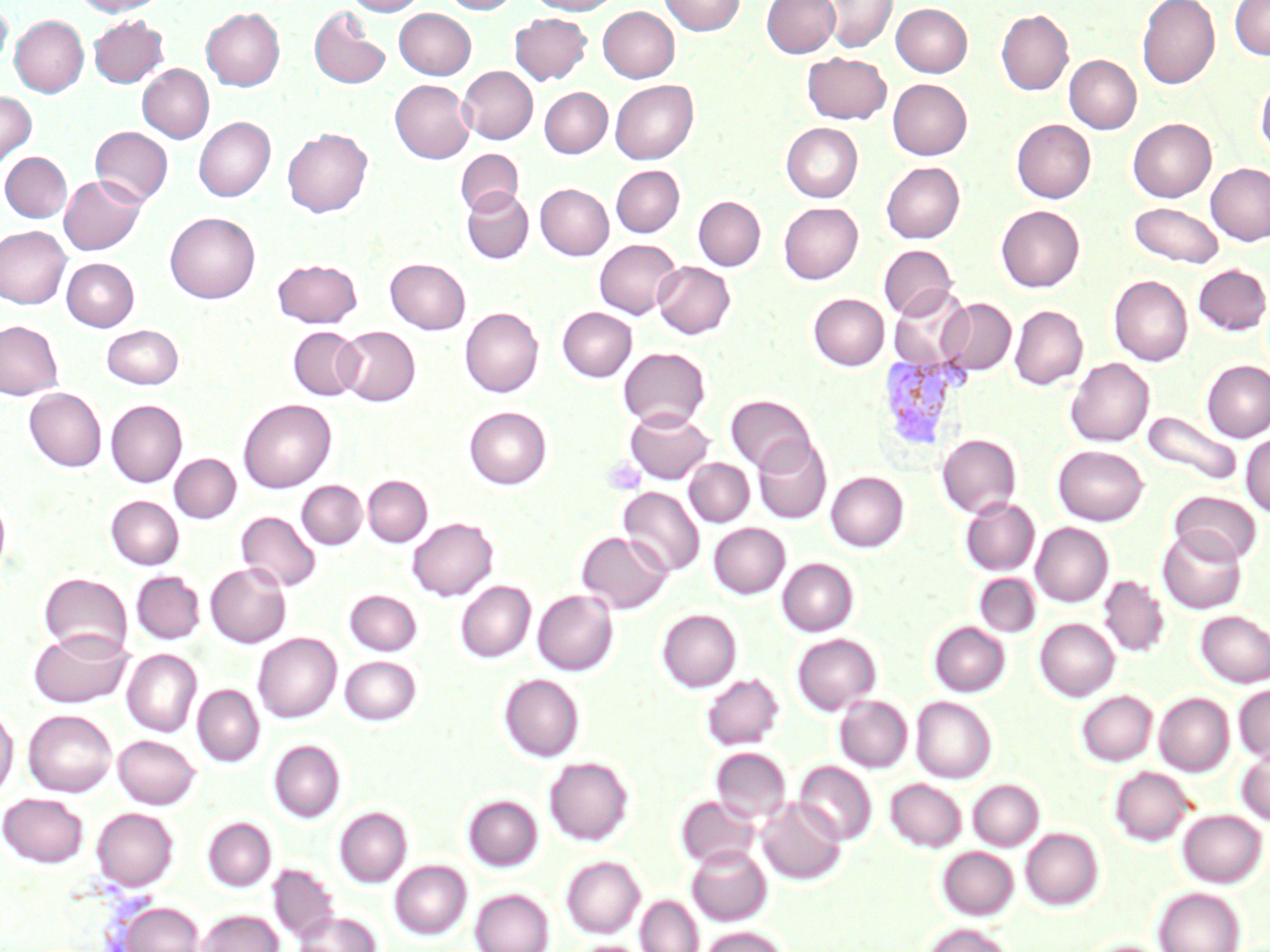

Summary:
  - Coordinate format: approximate bounding boxes as (x1,y1)-(x2,y2) corner pairs in pixels
  - Uninfected red blood cell locations: (73,0)-(168,16), (346,0)-(426,15), (441,0)-(520,14), (528,0)-(619,15), (660,0)-(745,35), (762,0)-(840,58), (822,0)-(897,52), (1136,0)-(1220,90), (1229,0)-(1270,60), (0,2)-(11,71), (891,3)-(972,76), (309,6)-(391,90), (202,7)-(285,91), (598,7)-(679,82), (394,8)-(475,79), (996,9)-(1073,95), (510,13)-(591,85), (10,15)-(88,97), (89,15)-(168,87), (803,52)-(892,124), (1064,55)-(1141,133), (137,64)-(213,142), (458,66)-(537,144), (1256,76)-(1270,162), (888,79)-(972,160), (390,80)-(474,163), (610,80)-(698,164), (540,87)-(612,158), (0,92)-(35,169), (194,117)-(275,201), (1128,118)-(1216,202), (1011,119)-(1095,203), (781,123)-(863,202), (90,126)-(173,206), (282,127)-(372,217), (456,149)-(523,216), (1,152)-(72,222), (881,162)-(965,243), (1206,163)-(1270,245), (611,165)-(684,237), (59,175)-(145,255), (535,183)-(613,260), (462,188)-(533,263), (693,197)-(765,270), (779,202)-(863,283), (1129,202)-(1224,268), (996,205)-(1084,292), (165,212)-(260,303), (0,226)-(71,308), (595,239)-(681,318), (879,244)-(957,319), (62,258)-(139,331), (272,258)-(362,328), (386,258)-(470,334), (653,261)-(735,338), (1194,264)-(1270,335), (1108,275)-(1193,365), (889,287)-(971,370), (808,294)-(889,370), (938,298)-(1016,375), (1010,305)-(1088,389), (460,307)-(543,397), (557,307)-(636,381), (0,321)-(63,399), (101,324)-(184,389), (336,326)-(420,406), (288,327)-(363,400), (618,347)-(710,429), (1066,358)-(1154,446), (1202,360)-(1270,442), (24,388)-(106,471), (726,394)-(817,473), (238,399)-(336,492), (106,400)-(187,487), (464,407)-(551,489), (625,408)-(714,484), (1143,410)-(1241,486), (937,434)-(1021,518), (1241,434)-(1270,517), (753,437)-(831,524), (1053,445)-(1148,525), (170,454)-(241,523), (684,459)-(754,526), (826,471)-(909,552), (363,475)-(432,546), (297,481)-(366,548), (618,486)-(705,577), (1170,491)-(1261,565), (0,495)-(10,580), (106,495)-(184,569), (961,497)-(1040,575), (236,511)-(322,592), (408,517)-(498,601), (709,523)-(790,598), (1031,523)-(1113,606), (1157,527)-(1247,614), (576,531)-(672,613), (777,558)-(858,636), (205,563)-(291,647), (131,571)-(205,644), (39,573)-(132,658), (975,574)-(1040,636), (1099,575)-(1170,657), (456,581)-(536,663), (345,590)-(422,655), (533,590)-(618,675), (657,609)-(742,692), (1197,610)-(1270,687), (1035,619)-(1119,700), (929,622)-(1010,696), (28,629)-(132,708), (253,633)-(341,722), (791,633)-(881,715), (122,649)-(201,736), (255,649)-(423,723), (340,655)-(421,725), (701,673)-(784,750), (499,674)-(584,762), (1234,684)-(1270,762), (193,685)-(264,767), (1077,691)-(1157,766), (1155,693)-(1234,776), (835,695)-(912,772), (911,697)-(996,783), (0,708)-(18,798), (23,710)-(117,796), (113,735)-(200,809), (269,740)-(345,822), (711,748)-(791,824), (1236,749)-(1270,825), (544,757)-(634,845), (794,761)-(877,845), (1110,766)-(1194,846), (886,779)-(966,852), (968,779)-(1044,850), (1,793)-(88,867), (463,795)-(542,871), (676,795)-(761,870), (756,797)-(846,885), (1,800)-(178,874), (334,807)-(412,887), (92,808)-(178,891), (1177,809)-(1267,887), (203,817)-(276,891), (1021,828)-(1103,910), (687,845)-(771,926), (937,846)-(1019,920), (561,856)-(645,938), (390,861)-(471,939), (268,864)-(338,944), (1154,887)-(1245,952), (470,888)-(554,952), (636,896)-(703,952), (117,901)-(204,952), (198,910)-(283,952), (293,911)-(380,952), (924,922)-(1015,952), (701,926)-(790,952), (1083,939)-(1168,952), (576,941)-(644,952)
  - Plasmodium vivax-infected red blood cell locations: (877,353)-(967,453)
  - Platelet locations: (604,456)-(645,496)
  - Slide-level diagnosis: Plasmodium vivax
  - Stain: May-Grünwald-Giemsa
  - Modality: light microscopy
  - Image size: 1270×952 pixels
  - Magnification: 1000x
  - Preparation: thin blood smear
  - Field of view: one of a larger specimen